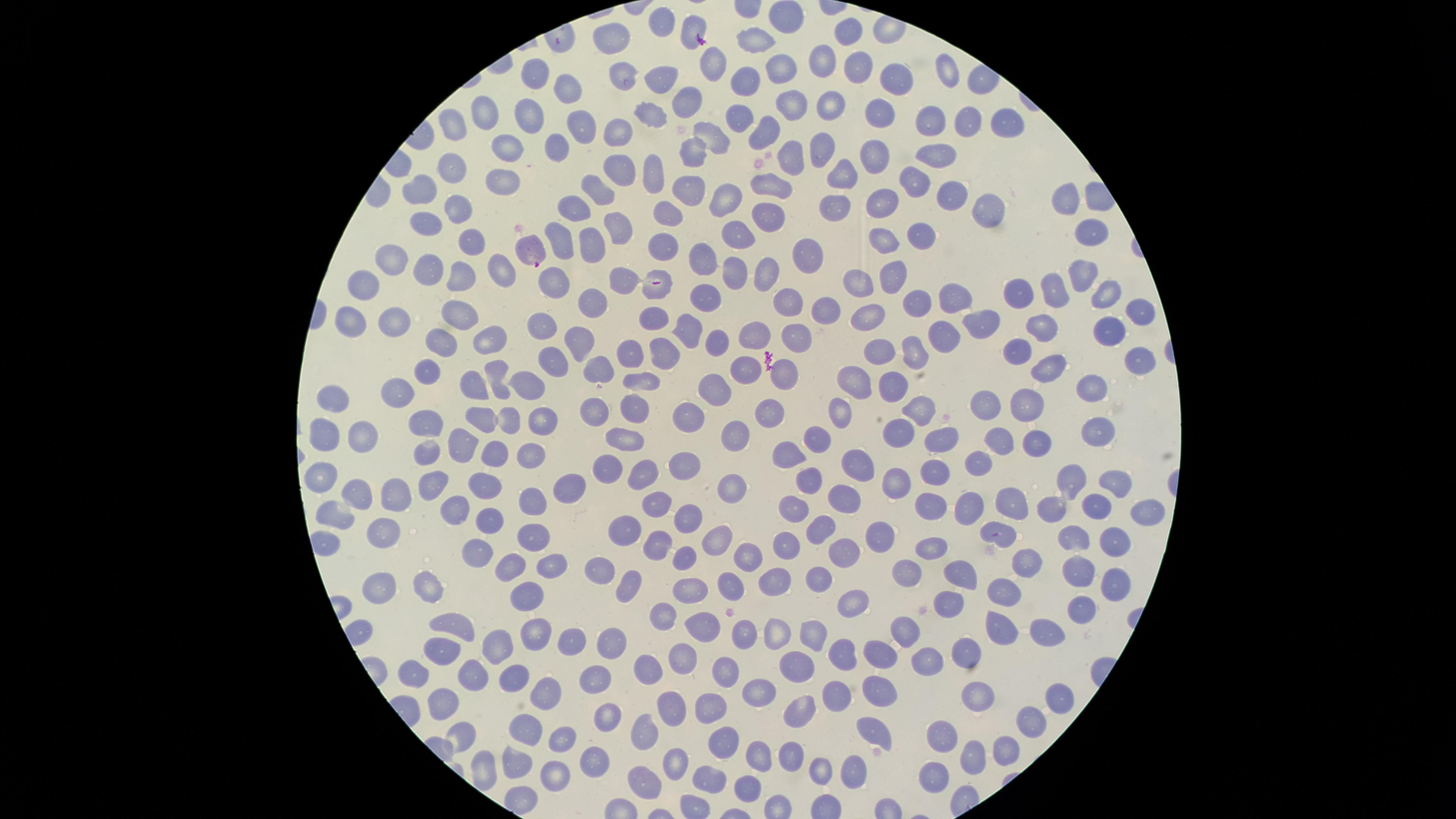 Approximate marker points as [x, y] in pixels. Parasitized red blood cells: [528, 249]. Uninfected red blood cells: [782, 22], [662, 25], [693, 28], [845, 34], [607, 41], [759, 42], [822, 61], [713, 64], [779, 66], [533, 70], [857, 70], [950, 72], [625, 77], [746, 78], [896, 79], [663, 81], [568, 88], [686, 102], [792, 108], [828, 108], [487, 112], [527, 113], [879, 114], [652, 116], [739, 116], [1002, 123], [930, 124], [967, 124], [453, 125], [580, 127], [614, 130], [762, 131], [713, 138], [557, 144], [505, 148], [690, 153], [939, 154], [820, 155], [793, 157], [877, 159], [450, 167], [614, 168], [654, 174], [842, 174], [913, 176], [496, 180], [769, 182], [594, 189], [420, 190], [685, 190], [728, 194], [953, 195], [1066, 201], [879, 202], [833, 207], [579, 208], [772, 209], [979, 209], [462, 210], [663, 214], [425, 225], [616, 227], [1084, 228], [738, 230], [916, 233], [467, 239], [884, 240], [589, 241], [558, 242], [666, 247], [702, 255], [809, 256], [395, 259], [427, 268], [889, 271], [1080, 271], [497, 273], [769, 275], [735, 276], [367, 279], [622, 280], [462, 282], [554, 282], [862, 282], [662, 286], [1058, 291], [1017, 292], [1102, 294], [707, 297], [957, 299], [915, 302], [587, 303], [781, 303], [457, 311], [824, 311], [1139, 311], [353, 316], [874, 318], [650, 320], [395, 322], [977, 322], [688, 325], [539, 326], [1042, 327], [1108, 327], [757, 333], [797, 334], [945, 336], [442, 337], [489, 337], [575, 342], [712, 343], [1016, 349], [879, 351], [916, 351], [631, 353], [665, 357], [1139, 357], [553, 358], [749, 364], [1052, 367], [591, 370], [424, 371], [784, 372], [495, 381], [645, 382], [1085, 383], [467, 384], [527, 384], [853, 384], [885, 384], [400, 389], [713, 390], [331, 393], [983, 406], [587, 408], [1026, 408], [634, 410], [773, 410], [839, 410], [916, 411], [543, 413], [692, 414], [483, 419], [424, 421], [506, 422], [1097, 427], [900, 433], [325, 434], [361, 435], [731, 436], [821, 436], [625, 437], [939, 438], [1003, 440], [1040, 441], [460, 443], [423, 450], [495, 451], [532, 451], [785, 454], [978, 460], [857, 461], [684, 462], [927, 468], [607, 470], [648, 474], [1069, 474], [319, 476], [431, 480], [481, 480], [810, 482], [1114, 483], [898, 486], [568, 487], [727, 490], [356, 491], [390, 492], [658, 498], [843, 498], [531, 500], [1013, 502], [1098, 503], [928, 504], [457, 505], [966, 505], [1052, 506], [793, 507], [1144, 512], [339, 513], [689, 515], [485, 518], [818, 526], [378, 531], [626, 533], [882, 533], [1000, 536], [534, 537], [654, 540], [714, 541], [1076, 541], [929, 547], [791, 548], [1113, 549], [837, 550], [682, 553], [746, 554], [470, 555], [1030, 557], [513, 559], [550, 559], [601, 565], [629, 573], [908, 573], [1077, 574], [962, 575], [818, 577], [770, 580], [727, 583], [376, 584], [1116, 586], [692, 588], [430, 589], [528, 589], [1001, 593], [852, 600], [950, 604], [1080, 610], [658, 618], [706, 623], [454, 626], [997, 629], [741, 630], [907, 630], [531, 631], [815, 631], [1046, 632], [778, 634], [571, 639], [494, 644], [609, 647], [841, 648], [438, 653], [965, 654], [884, 657], [924, 661], [678, 664], [795, 666], [726, 670], [474, 671], [642, 671], [411, 672], [514, 674], [592, 680], [883, 688], [977, 688], [758, 690], [538, 691], [834, 691], [1064, 696], [444, 703], [709, 706], [799, 712], [674, 713], [605, 719], [1021, 725], [525, 728], [873, 728], [646, 732], [562, 737], [463, 738], [942, 739], [721, 741], [1001, 748], [970, 752], [760, 754], [592, 755], [789, 757], [673, 759], [511, 761], [555, 767], [483, 770], [855, 774], [709, 775], [819, 776], [646, 778], [927, 780], [748, 786]. The visible region is circular. Thin blood smear. Species: Plasmodium falciparum. Image is 1456×819 pixels. Smartphone photograph through the microscope eyepiece. One field of view of the specimen. Presence: malaria parasites seen. Giemsa-stained preparation.